Locate every blood parasite and identify its species.
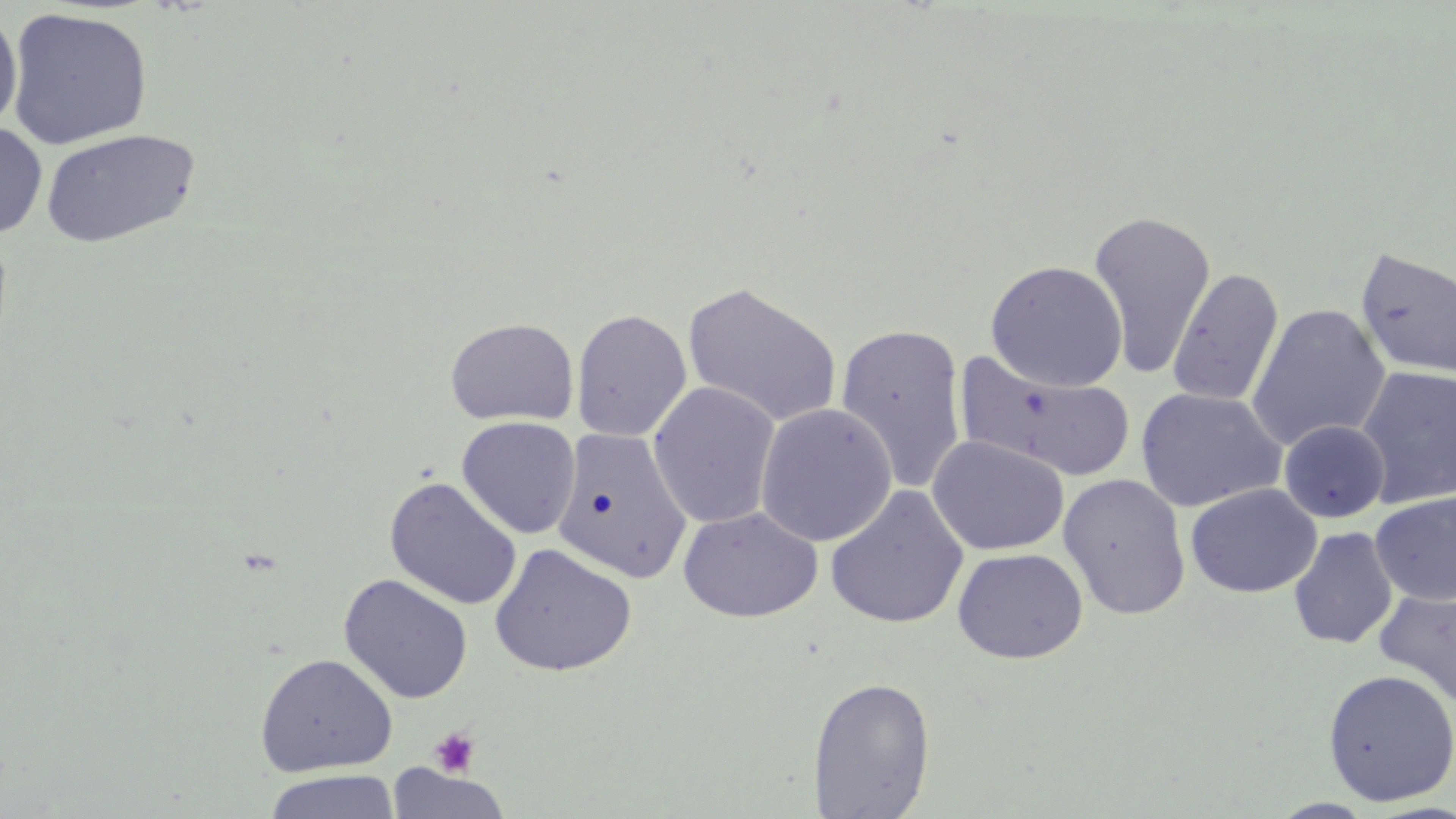
No blood parasites seen.

Approximate bounding boxes as (x1, y1, x2, y2) in pixels. Platelet locations: (429, 727, 481, 778). Uninfected red blood cell locations: (5, 7, 153, 149), (0, 9, 23, 133), (0, 121, 47, 238), (40, 127, 201, 248), (1087, 209, 1215, 379), (1355, 245, 1456, 381), (985, 260, 1128, 392), (1167, 268, 1284, 408), (682, 281, 843, 428), (1247, 303, 1390, 451), (571, 309, 692, 442), (445, 317, 579, 426), (834, 323, 968, 495), (957, 352, 1137, 483), (1355, 365, 1456, 509), (647, 381, 781, 529), (1135, 387, 1287, 512), (755, 402, 897, 547), (456, 416, 581, 539), (1279, 420, 1390, 523), (552, 429, 693, 584), (927, 434, 1070, 555), (1058, 472, 1191, 620), (384, 477, 523, 610), (1185, 483, 1322, 598), (824, 485, 969, 630), (1371, 492, 1456, 606), (678, 506, 822, 622), (1288, 526, 1399, 649), (489, 543, 637, 677), (952, 547, 1088, 664), (338, 574, 473, 703), (1374, 588, 1456, 707), (254, 652, 397, 776), (1322, 669, 1456, 806), (808, 677, 936, 818), (386, 764, 511, 819), (263, 770, 400, 819), (1268, 798, 1378, 818). Slide-level diagnosis: negative for blood parasites. Captured at 1000x magnification. Light microscopy. May-Grünwald-Giemsa stain. One field of a larger specimen. Image is 1456×819 pixels. Thin blood film.